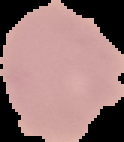

Result: no malaria parasites seen. From a thin blood smear. Image is 124×142 pixels. The area outside the segmented cell region is set to black.